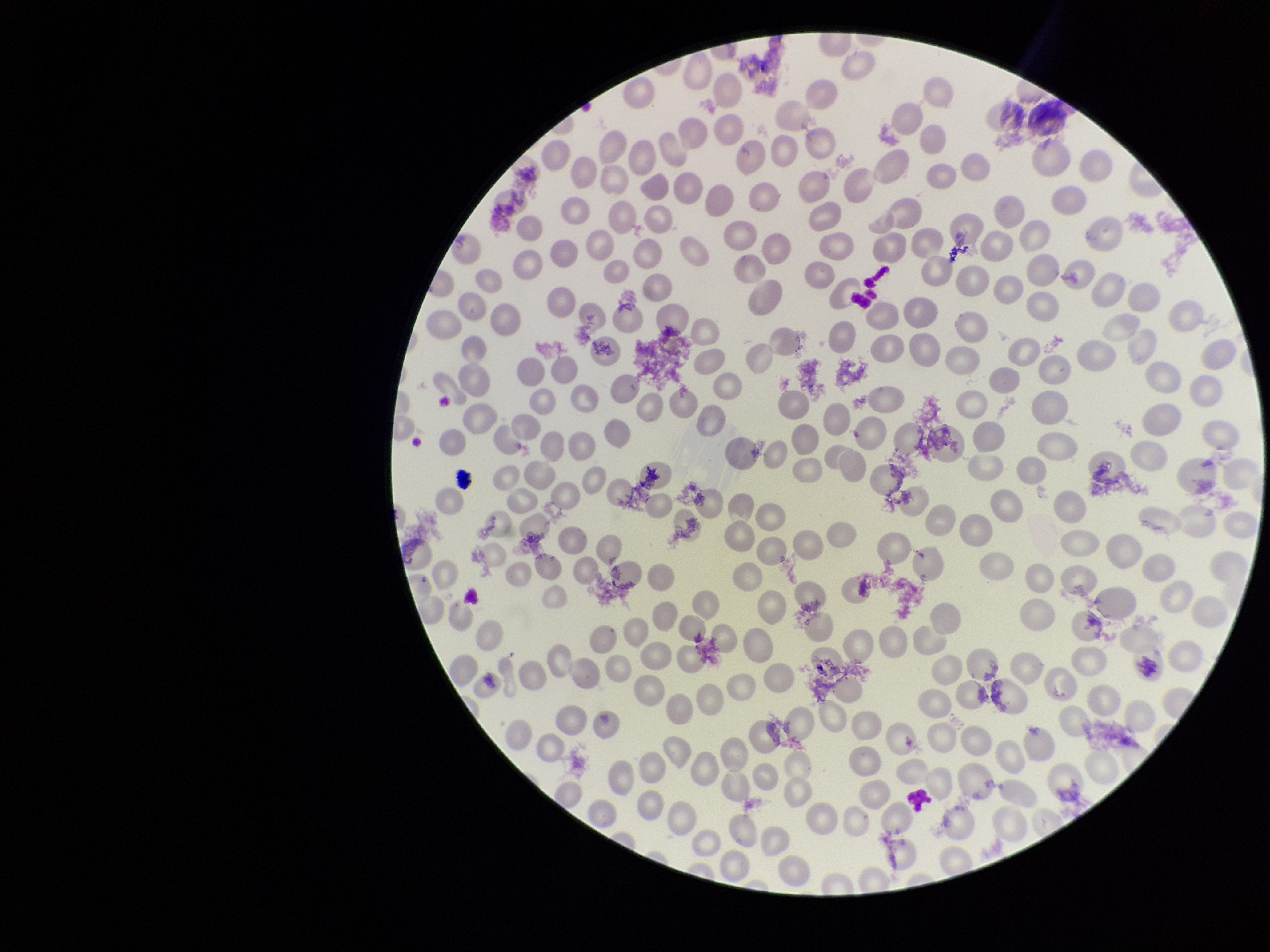
parasitized red blood cells = none detected
red blood cell count = 245
preparation = thin smear
parasitized red blood cell count = 0
image size = 1270×952 pixels
patient malaria status = negative
stain = Giemsa
field of view = single
capture = smartphone photograph through the microscope eyepiece